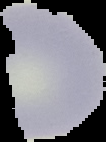
preparation = thin blood smear
image size = 106×142 pixels
result = no malaria parasites seen
image type = cell region segmented out of the field of view; surrounding area masked to black